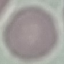

result = negative for malaria parasites
image type = cell patch, automatically extracted from a larger field of view and resized to 64 × 64 pixels
capture = smartphone camera at the microscope eyepiece
stain = Giemsa
preparation = thin smear